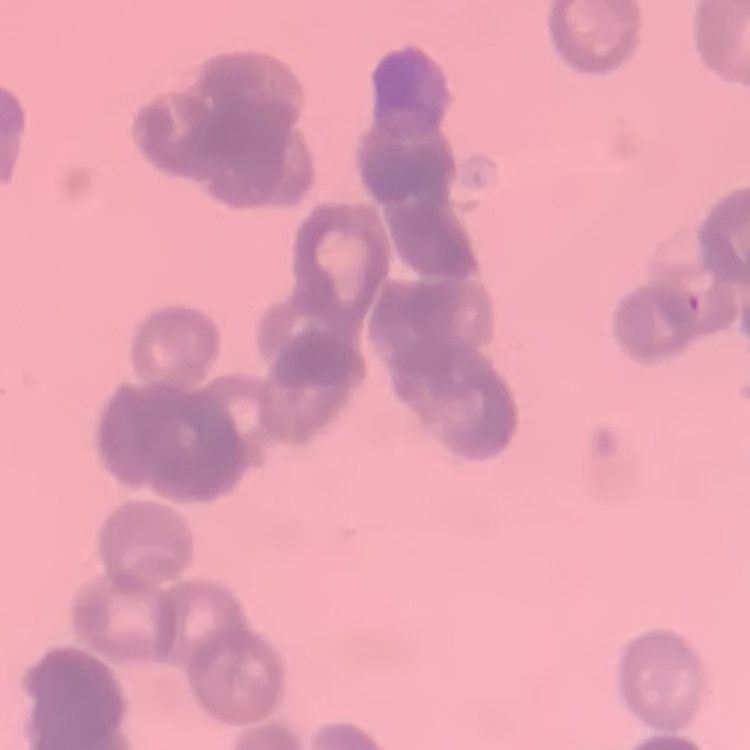 The red blood cells exhibit rouleaux formation. Thin peripheral smear. Stained with either Field's or Giemsa. One tile cut from a larger photomicrograph.